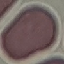

Malaria status: uninfected. Cell patch, automatically extracted from a larger field of view and resized to 64 × 64 pixels. Giemsa stain. Thin blood film. Photographed with a smartphone camera at the microscope eyepiece.